Report the malaria status of this cell.
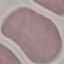
Uninfected.

{
  "image_type": "automatically extracted cell patch, resized to 64 × 64 pixels",
  "capture": "smartphone camera at the microscope eyepiece",
  "stain": "Giemsa",
  "preparation": "thin blood smear"
}